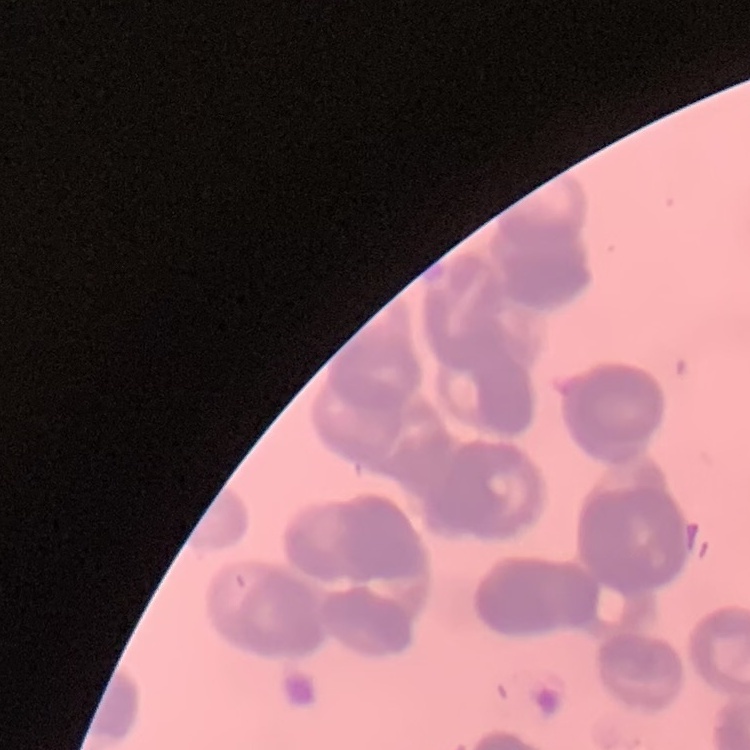

The erythrocytes exhibit rouleaux formation. Thin blood smear. One tile cut from a larger photomicrograph. Field's or Giemsa stain.